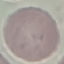

Malaria status: uninfected. Automatically extracted cell patch, resized to 64 × 64 pixels. Thin smear of blood. Acquired by smartphone through the microscope eyepiece. Giemsa stain.